Report the malaria status of this cell.
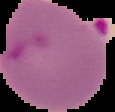

It is parasitized.

preparation = thin blood smear
image size = 115×112 pixels
image type = segmented cell region with the area outside set to black